Report the malaria status of this cell.
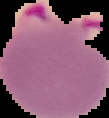

Parasitized.

image size = 109×118 pixels
preparation = thin blood smear
image type = cell region segmented out of the field of view; surrounding area masked to black